Assess this cell for malaria.
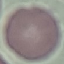
It is uninfected.

preparation = thin blood film
stain = Giemsa
capture = smartphone through the microscope eyepiece
image type = cell patch, automatically extracted from a larger field of view and resized to 64 × 64 pixels